Locate every uninfected red blood cell.
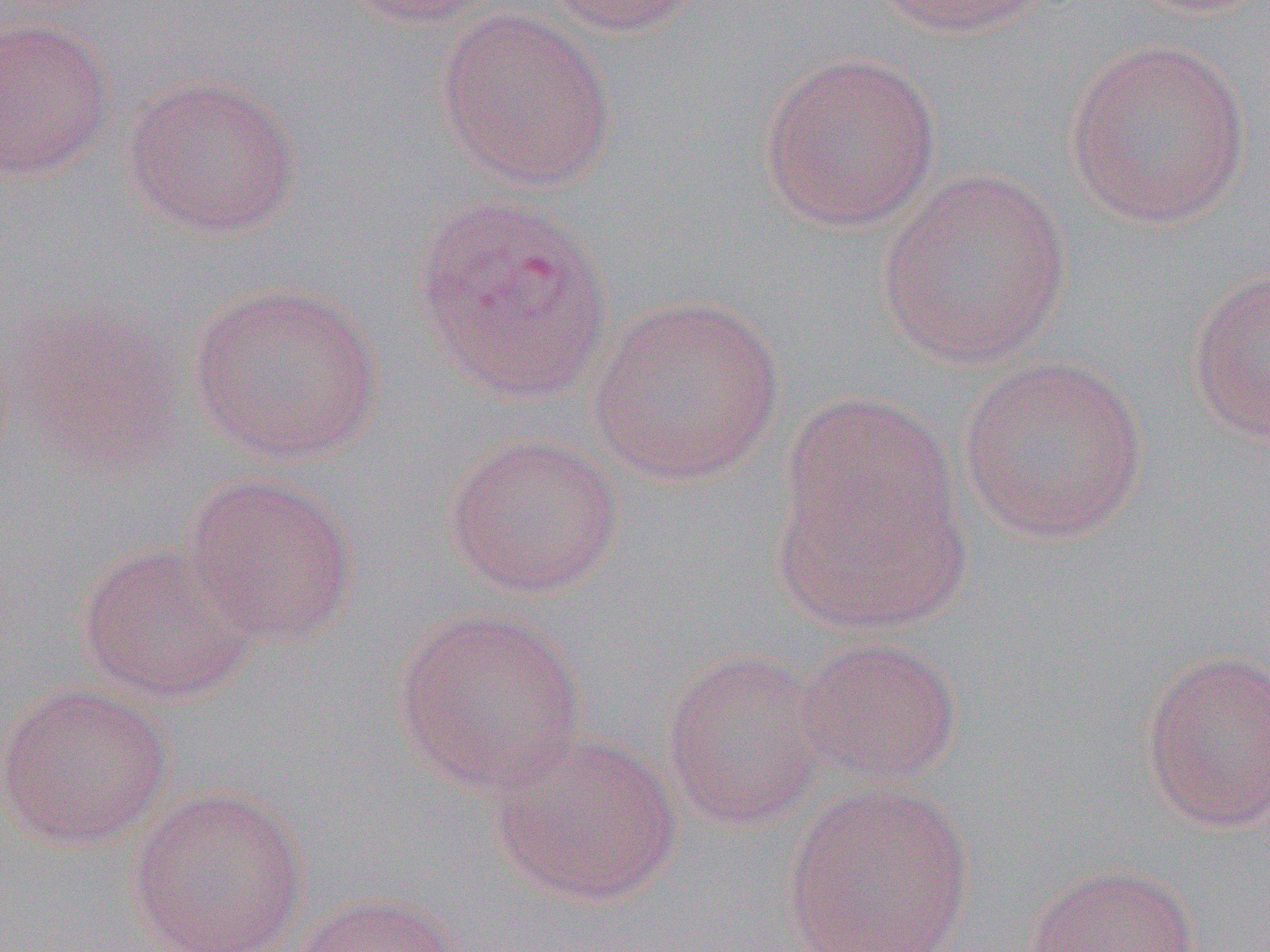
Approximate bounding boxes as (x1,y1)-(x2,y2) corner pairs in pixels.
Uninfected red blood cells: (331,0)-(507,28), (533,0)-(702,37), (869,0)-(1050,38), (434,8)-(617,191), (0,15)-(117,181), (1063,38)-(1253,228), (757,50)-(942,233), (121,73)-(302,239), (875,169)-(1073,370), (412,192)-(613,405), (1186,264)-(1270,448), (186,279)-(384,465), (587,292)-(785,486), (957,354)-(1149,545), (771,412)-(969,637), (444,432)-(624,599), (181,470)-(358,646), (76,538)-(261,705), (393,605)-(587,795), (793,637)-(962,788), (659,647)-(831,831), (1138,647)-(1270,833), (0,683)-(173,849), (488,729)-(682,907), (779,778)-(976,952), (127,783)-(309,952), (1021,863)-(1202,951), (284,892)-(466,952).

Summary:
  - Slide-level diagnosis: Plasmodium vivax
  - Magnification: 1000x
  - Preparation: thin blood film
  - Field of view: single
  - Image size: 1270×952 pixels
  - Modality: light microscopy